Give the position of every malaria parasite.
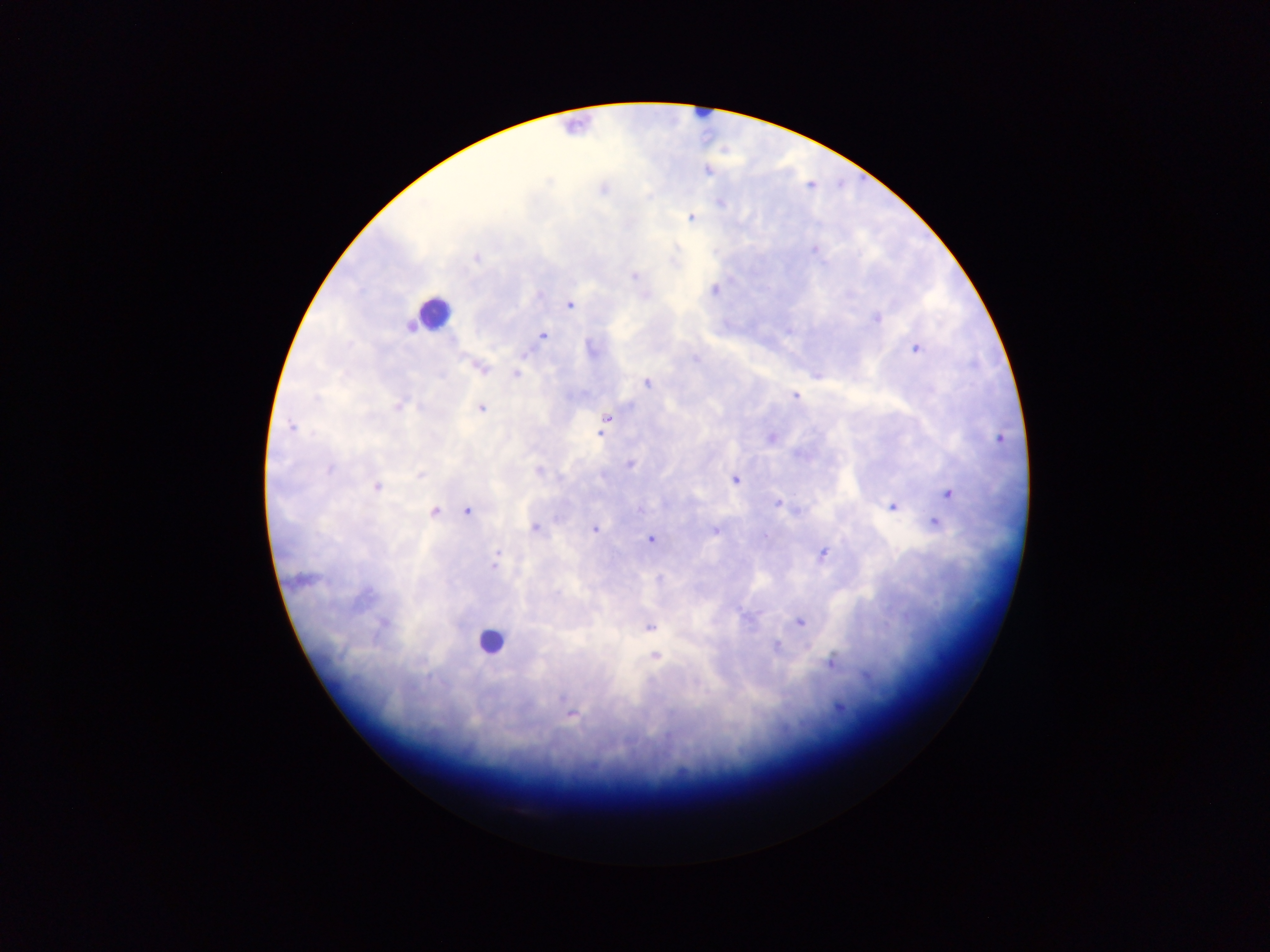

Approximate centers as {x, y} in pixels.
Malaria parasites: {603, 188}, {691, 217}, {477, 258}, {634, 277}, {714, 289}, {569, 304}, {876, 319}, {542, 336}, {590, 347}, {916, 348}, {478, 366}, {516, 374}, {819, 375}, {647, 382}, {795, 396}, {399, 404}, {480, 408}, {606, 418}, {291, 427}, {603, 427}, {771, 437}, {630, 464}, {734, 479}, {376, 487}, {947, 494}, {778, 503}, {892, 505}, {467, 510}, {433, 511}, {933, 521}, {535, 527}, {594, 528}, {715, 529}, {651, 538}, {822, 554}, {495, 564}, {799, 621}, {648, 626}, {655, 656}, {831, 661}, {838, 707}, {571, 712}.

{
  "image_size": "1270×952 pixels",
  "preparation": "thick blood smear",
  "field_of_view": "single",
  "capture": "mobile-phone photograph through a microscope",
  "leukocyte_locations": "approximate centers as {x, y} in pixels: {432, 312}, {490, 641}",
  "country": "Ghana"
}